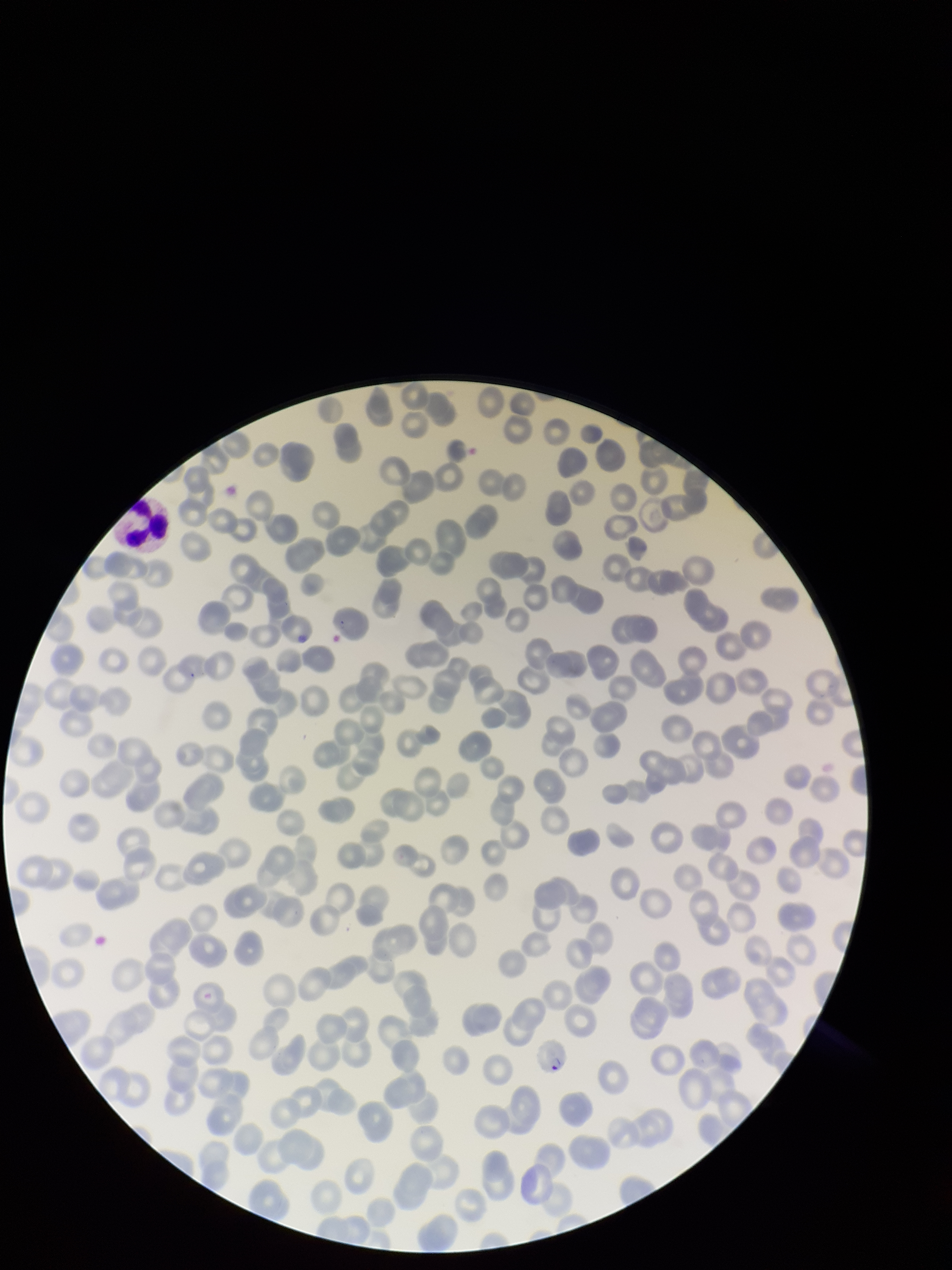
parasitized red blood cell count = 1
species reported for this patient = Plasmodium falciparum
red blood cell count = 204
patient malaria status = infected
field of view = single
parasitized red blood cells = identified
preparation = thin
capture = smartphone photograph through the microscope eyepiece
stain = Giemsa
image size = 952×1270 pixels